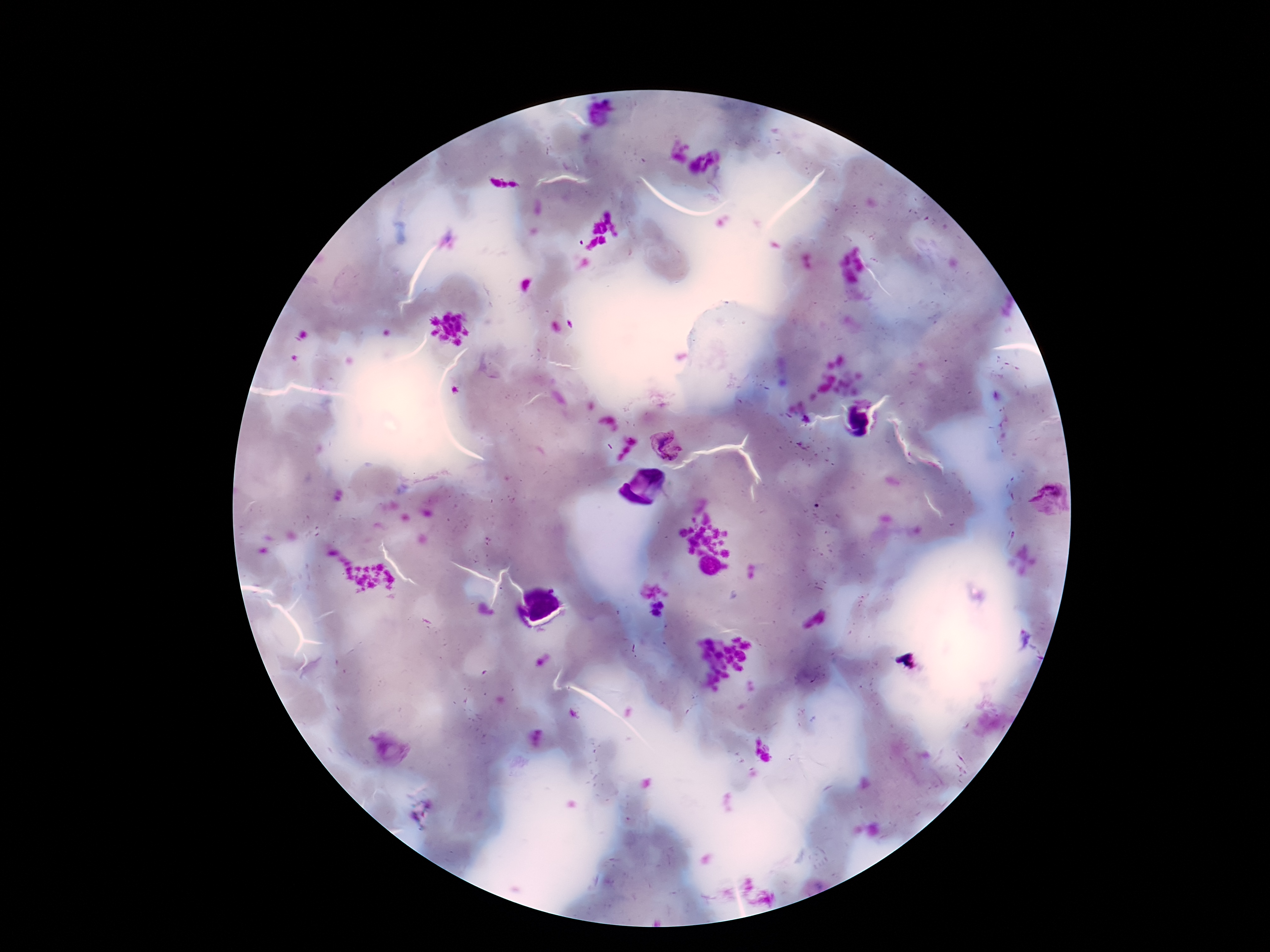
magnification: 100x
preparation: thick blood smear
capture: smartphone camera through the microscope eyepiece
stain: Giemsa
image_size: 1270×952 pixels
patient_malaria_status: infected
plasmodium_parasite_locations: 'approximate centers as [x, y] in pixels: [703, 161], [668, 443], [1049, 499], [386, 749]'
field_of_view: one from this slide